Identify the blood parasite species.
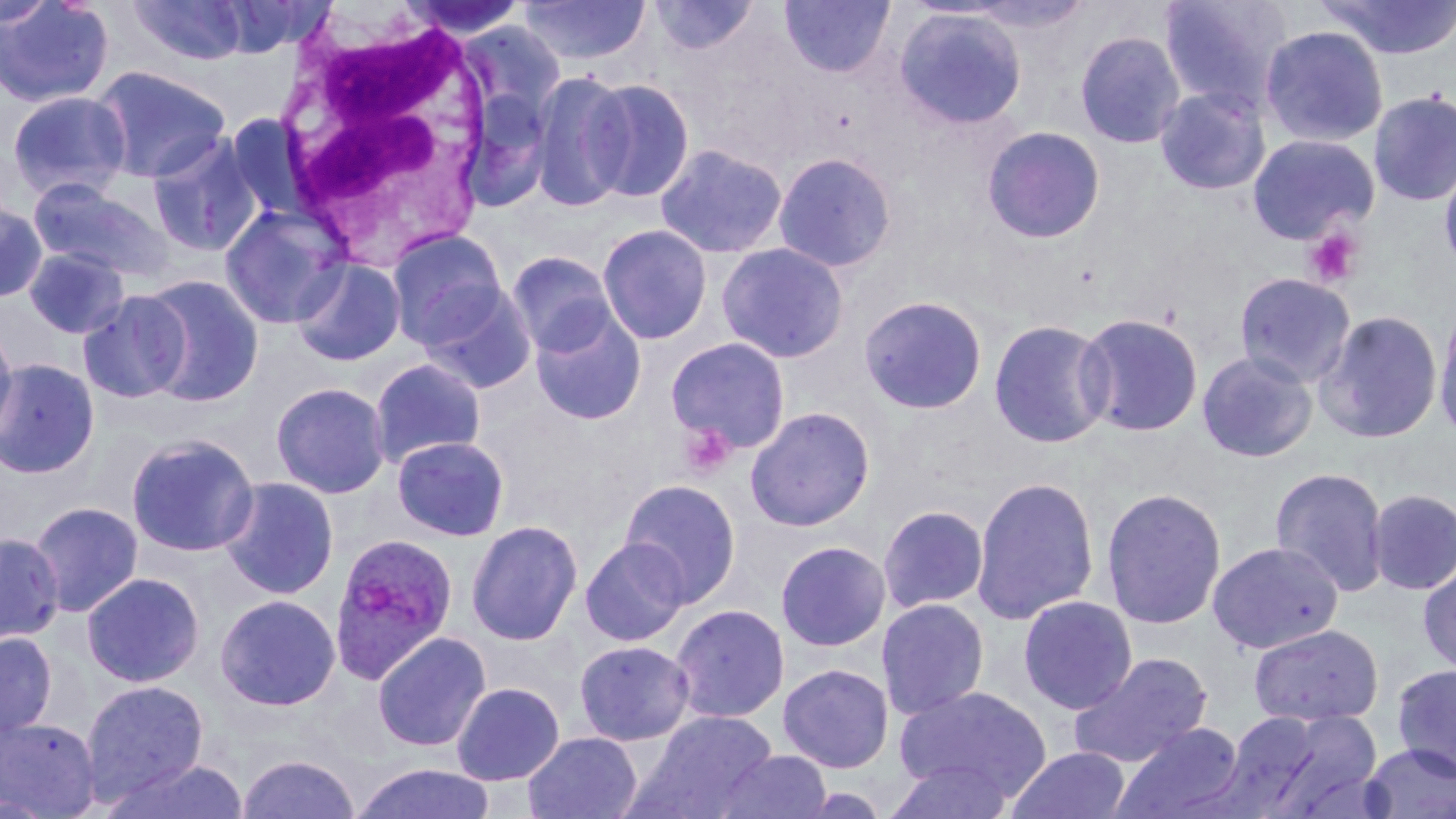

Plasmodium ovale.

Approximate bounding boxes as [x1, y1, x2, y2] in pixels. Plasmodium ovale-infected red blood cell locations: [329, 532, 458, 683]. Uninfected red blood cell locations: [0, 0, 116, 109], [214, 0, 335, 58], [398, 0, 531, 40], [518, 0, 651, 65], [648, 0, 760, 56], [778, 0, 896, 79], [1159, 0, 1295, 113], [1314, 0, 1456, 61], [0, 1, 58, 29], [127, 1, 251, 66], [894, 7, 1028, 130], [1259, 25, 1389, 148], [1075, 30, 1185, 149], [90, 65, 232, 183], [529, 70, 633, 213], [584, 78, 696, 203], [1155, 86, 1271, 196], [459, 87, 555, 213], [6, 90, 132, 202], [1368, 91, 1456, 207], [226, 114, 311, 220], [981, 126, 1106, 244], [1247, 133, 1379, 244], [147, 134, 265, 257], [654, 142, 788, 259], [773, 151, 897, 274], [1439, 160, 1456, 277], [28, 178, 175, 283], [0, 199, 49, 303], [219, 203, 350, 329], [597, 224, 713, 345], [387, 229, 508, 347], [716, 242, 849, 363], [23, 246, 130, 339], [506, 251, 617, 357], [290, 257, 406, 366], [1233, 272, 1356, 388], [139, 274, 265, 407], [417, 282, 538, 395], [78, 290, 191, 404], [859, 295, 988, 415], [1433, 300, 1456, 443], [530, 308, 647, 425], [1314, 309, 1444, 445], [1074, 312, 1204, 437], [988, 318, 1114, 450], [0, 321, 18, 444], [665, 337, 791, 455], [1196, 350, 1318, 463], [369, 357, 486, 467], [0, 358, 100, 479], [271, 381, 391, 498], [744, 406, 876, 532], [125, 433, 259, 558], [392, 436, 509, 541], [1269, 466, 1391, 598], [971, 475, 1100, 625], [218, 476, 339, 600], [618, 478, 741, 607], [1101, 487, 1227, 630], [1367, 488, 1456, 595], [28, 501, 144, 618], [877, 504, 989, 615], [466, 519, 583, 646], [0, 532, 63, 645], [579, 538, 690, 647], [775, 540, 891, 651], [1207, 540, 1344, 654], [1417, 557, 1456, 676], [81, 571, 205, 688], [214, 594, 341, 712], [1017, 595, 1138, 715], [876, 597, 990, 720], [669, 603, 790, 724], [1247, 623, 1384, 727], [0, 631, 58, 740], [372, 631, 492, 752], [574, 640, 695, 746], [1069, 652, 1213, 767], [778, 663, 894, 773], [1390, 663, 1456, 779], [81, 679, 209, 803], [451, 682, 565, 785], [892, 685, 1051, 805], [631, 711, 778, 818], [1219, 711, 1329, 813], [1256, 712, 1386, 819], [1, 715, 101, 818], [1111, 721, 1247, 819], [523, 731, 642, 819], [1360, 742, 1456, 819], [1007, 747, 1132, 819], [714, 749, 833, 819], [236, 753, 360, 818], [98, 756, 250, 819], [885, 759, 1014, 819], [349, 762, 497, 819]. White blood cell locations: [271, 6, 498, 262]. Platelet locations: [1303, 228, 1363, 288], [679, 422, 737, 479]. 1000x magnification. May-Grünwald-Giemsa-stained preparation. Light microscopy. Thin blood smear. Image is 1456×819 pixels. Single field of view.